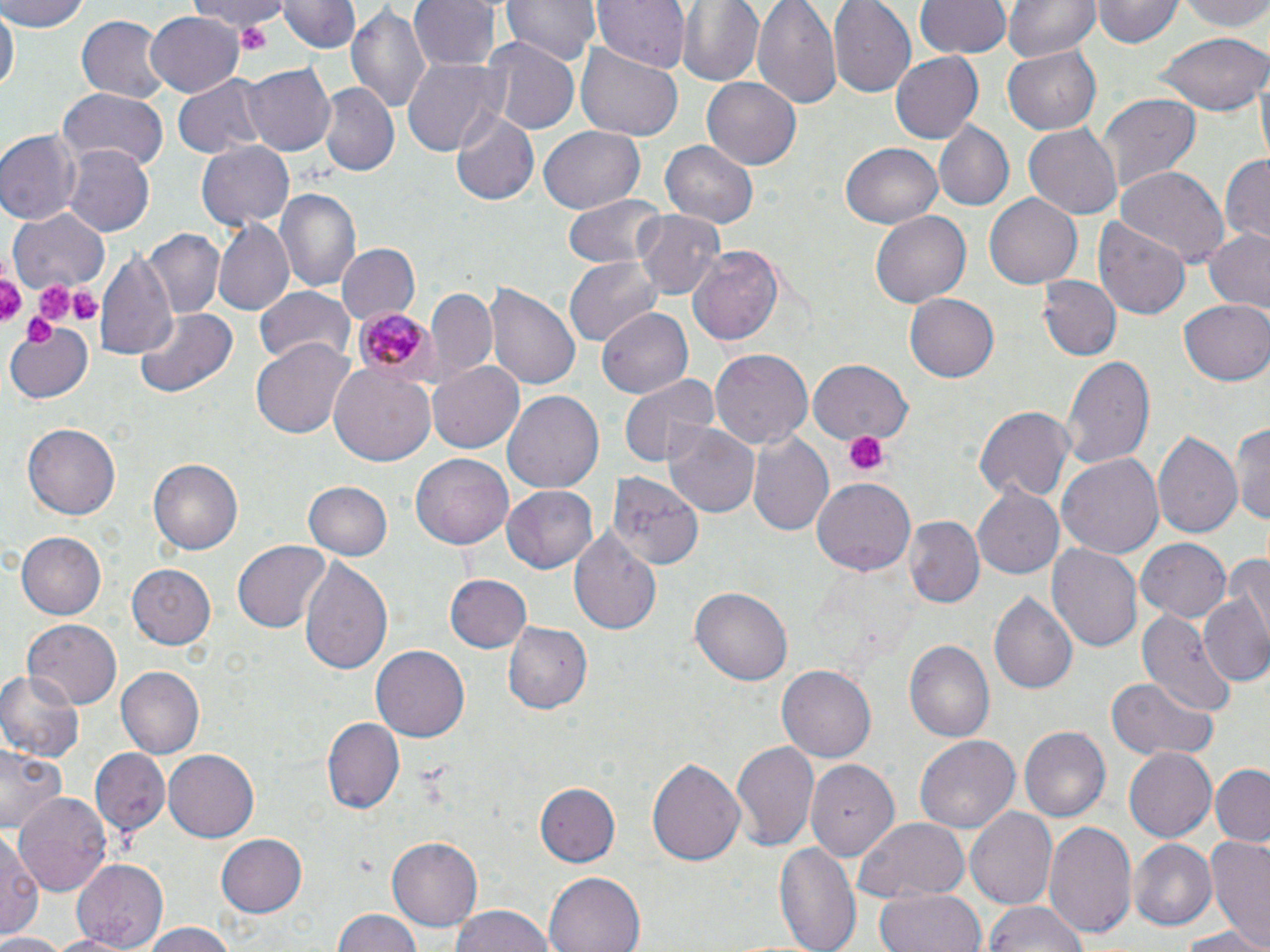

Approximate bounding boxes as (x1,y1)-(x2,y2) corner pairs in pixels. Uninfected red blood cell locations: (1,0)-(90,32), (194,0)-(287,37), (281,0)-(357,53), (410,0)-(497,71), (503,0)-(598,67), (593,0)-(688,74), (677,0)-(765,86), (753,0)-(843,111), (828,0)-(916,98), (917,0)-(1009,59), (1003,0)-(1099,64), (1093,0)-(1180,50), (1181,0)-(1270,35), (346,3)-(432,118), (1,7)-(16,97), (147,11)-(245,95), (73,15)-(168,104), (1151,31)-(1268,116), (479,36)-(579,135), (575,43)-(682,144), (1002,44)-(1100,134), (890,53)-(983,143), (400,58)-(505,158), (242,63)-(335,156), (173,74)-(266,160), (703,76)-(800,170), (318,85)-(398,176), (58,86)-(171,172), (1095,93)-(1200,194), (453,110)-(539,207), (934,120)-(1013,212), (1023,123)-(1122,217), (0,127)-(80,226), (538,127)-(645,213), (197,140)-(294,232), (661,140)-(756,227), (839,142)-(944,228), (65,147)-(153,235), (1219,153)-(1269,247), (1114,165)-(1229,268), (275,186)-(360,291), (985,193)-(1082,289), (562,195)-(666,272), (10,207)-(109,293), (869,209)-(973,308), (632,210)-(726,300), (1093,216)-(1190,319), (212,221)-(295,315), (140,228)-(224,318), (1202,229)-(1270,319), (334,243)-(420,327), (687,243)-(787,349), (96,249)-(179,365), (563,255)-(662,344), (1040,277)-(1120,362), (485,282)-(582,391), (254,286)-(356,366), (426,287)-(498,385), (905,290)-(1003,382), (1180,299)-(1270,386), (135,306)-(239,398), (597,309)-(693,397), (4,320)-(97,402), (252,338)-(355,439), (708,348)-(813,452), (1063,355)-(1154,471), (426,360)-(525,453), (807,360)-(914,442), (330,362)-(435,466), (617,372)-(716,468), (502,389)-(603,497), (973,407)-(1073,505), (1231,418)-(1270,527), (664,421)-(759,520), (23,423)-(119,520), (1153,429)-(1243,543), (746,431)-(836,539), (1056,453)-(1165,562), (411,454)-(514,549), (148,457)-(244,555), (607,471)-(705,569), (811,476)-(915,574), (303,481)-(394,562), (502,486)-(599,573), (973,486)-(1067,580), (903,518)-(984,611), (569,526)-(663,638), (16,531)-(108,619), (1135,539)-(1230,623), (234,541)-(330,631), (1048,542)-(1143,655), (1226,549)-(1270,647), (298,556)-(394,679), (127,566)-(215,649), (443,575)-(531,653), (690,587)-(791,687), (991,591)-(1077,697), (1201,596)-(1270,687), (1136,610)-(1235,713), (23,619)-(120,710), (502,619)-(593,713), (904,640)-(995,744), (371,645)-(468,743), (777,665)-(877,762), (0,667)-(84,761), (117,667)-(204,757), (1106,677)-(1218,761), (322,718)-(402,814), (1020,726)-(1110,822), (915,734)-(1022,833), (732,741)-(819,854), (0,744)-(67,835), (1122,747)-(1215,842), (89,749)-(171,836), (164,751)-(259,842), (646,756)-(746,866), (806,763)-(893,868), (1210,765)-(1270,847), (535,782)-(620,868), (16,793)-(111,897), (0,800)-(76,917), (964,806)-(1057,910), (853,818)-(972,903), (1042,819)-(1137,942), (0,826)-(41,944), (216,831)-(307,918), (388,835)-(482,931), (1206,836)-(1270,949), (1129,837)-(1216,930), (774,840)-(861,952), (70,859)-(168,950), (544,872)-(646,952), (876,889)-(985,952), (984,900)-(1087,952), (447,905)-(557,952), (333,909)-(422,951), (134,922)-(246,951), (1174,926)-(1270,952), (41,933)-(140,952), (0,934)-(65,952). Plasmodium malariae-infected red blood cell locations: (352,304)-(436,385). Platelet locations: (233,20)-(274,48), (0,267)-(25,323), (30,275)-(77,329), (69,288)-(102,322), (23,312)-(57,350), (845,430)-(887,477). Slide-level diagnosis: Plasmodium malariae. Light microscopy. 1000x magnification. Image is 1270×952 pixels. Single field of view. Thin blood smear. May-Grünwald-Giemsa-stained preparation.